Point out each malaria parasite.
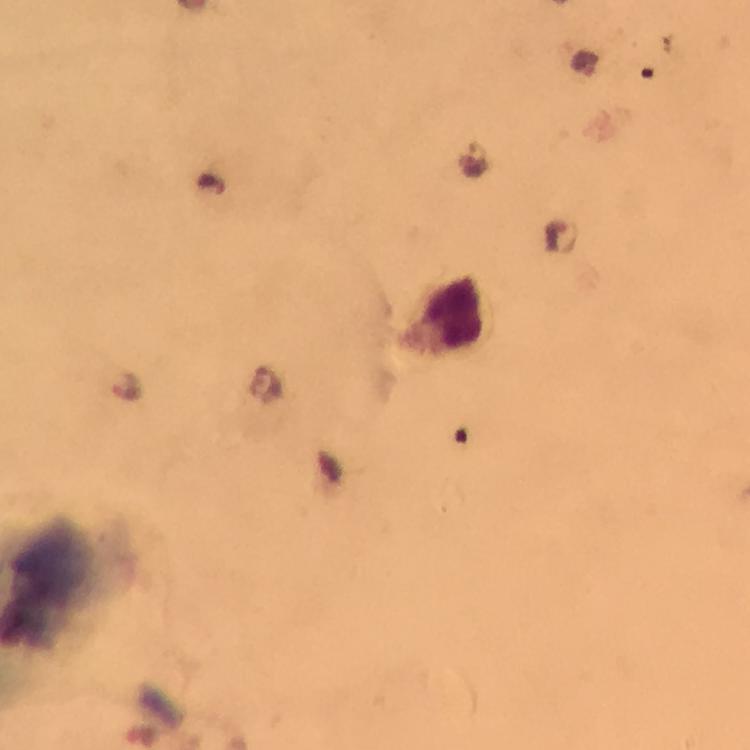

Approximate centers as (x, y) in pixels.
Malaria parasites: (475, 157), (210, 183), (561, 239), (127, 385).

capture: smartphone camera through the microscope
preparation: thick blood smear
cropped_from: one field of view
magnification: 100x
image_size: 750×750 pixels
stain: Giemsa
context: from a diagnostic examination for malaria
immersion_oil: applied